Outline each blood parasite and name the species.
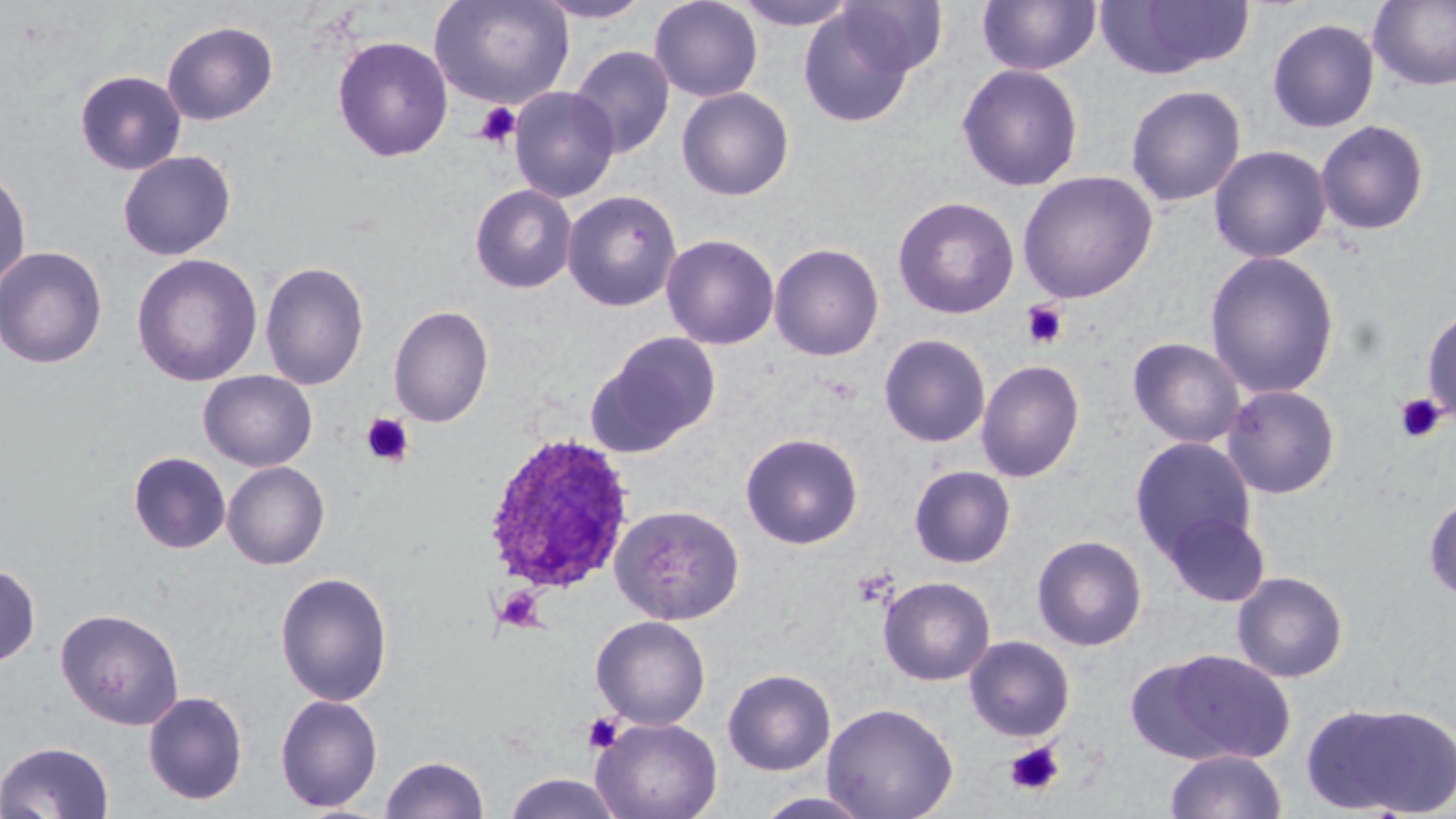
Approximate bounding boxes as named x1/y1/x2/y2 corners in pixels.
Plasmodium ovale-infected red blood cells: (x1=480, y1=432, x2=637, y2=599).
No Plasmodium falciparum, Plasmodium malariae, Plasmodium vivax, Babesia divergens, or Trypanosoma brucei observed.

slide_level_diagnosis: Plasmodium ovale
preparation: thin blood film
uninfected_red_blood_cell_locations: 'approximate bounding boxes as named x1/y1/x2/y2 corners in pixels: (x1=428, y1=0, x2=575, y2=109), (x1=532, y1=0, x2=653, y2=24), (x1=649, y1=0, x2=763, y2=102), (x1=734, y1=0, x2=860, y2=30), (x1=836, y1=0, x2=948, y2=79), (x1=977, y1=0, x2=1101, y2=76), (x1=1096, y1=0, x2=1254, y2=79), (x1=1368, y1=0, x2=1456, y2=91), (x1=797, y1=7, x2=916, y2=127), (x1=1267, y1=18, x2=1380, y2=133), (x1=162, y1=20, x2=278, y2=125), (x1=332, y1=35, x2=453, y2=162), (x1=569, y1=45, x2=675, y2=159), (x1=956, y1=63, x2=1084, y2=192), (x1=75, y1=70, x2=187, y2=175), (x1=1125, y1=84, x2=1246, y2=207), (x1=509, y1=86, x2=619, y2=203), (x1=676, y1=87, x2=795, y2=200), (x1=1315, y1=119, x2=1430, y2=236), (x1=1209, y1=145, x2=1331, y2=263), (x1=118, y1=150, x2=236, y2=261), (x1=0, y1=166, x2=31, y2=295), (x1=1017, y1=170, x2=1158, y2=304), (x1=470, y1=184, x2=577, y2=293), (x1=562, y1=190, x2=683, y2=312), (x1=892, y1=195, x2=1020, y2=319), (x1=661, y1=234, x2=780, y2=350), (x1=768, y1=242, x2=885, y2=361), (x1=0, y1=245, x2=108, y2=369), (x1=1204, y1=250, x2=1340, y2=399), (x1=131, y1=253, x2=263, y2=387), (x1=260, y1=260, x2=369, y2=390), (x1=1422, y1=303, x2=1456, y2=430), (x1=388, y1=305, x2=494, y2=427), (x1=588, y1=331, x2=723, y2=455), (x1=878, y1=333, x2=991, y2=448), (x1=1128, y1=337, x2=1245, y2=448), (x1=975, y1=359, x2=1086, y2=482), (x1=198, y1=370, x2=317, y2=471), (x1=1221, y1=384, x2=1341, y2=499), (x1=740, y1=432, x2=864, y2=550), (x1=1129, y1=437, x2=1257, y2=563), (x1=128, y1=451, x2=231, y2=554), (x1=222, y1=461, x2=330, y2=569), (x1=909, y1=465, x2=1016, y2=568), (x1=1423, y1=494, x2=1456, y2=602), (x1=609, y1=504, x2=745, y2=626), (x1=1161, y1=511, x2=1272, y2=606), (x1=1032, y1=534, x2=1147, y2=651), (x1=0, y1=561, x2=41, y2=668), (x1=1232, y1=570, x2=1349, y2=683), (x1=275, y1=571, x2=394, y2=707), (x1=878, y1=575, x2=995, y2=685), (x1=55, y1=607, x2=185, y2=730), (x1=591, y1=615, x2=711, y2=729), (x1=963, y1=635, x2=1075, y2=742), (x1=1151, y1=648, x2=1296, y2=763), (x1=723, y1=668, x2=836, y2=776), (x1=143, y1=690, x2=248, y2=805), (x1=275, y1=693, x2=383, y2=813), (x1=1304, y1=700, x2=1456, y2=817), (x1=822, y1=702, x2=959, y2=819), (x1=590, y1=717, x2=723, y2=819), (x1=0, y1=740, x2=114, y2=819), (x1=1164, y1=749, x2=1287, y2=819), (x1=380, y1=754, x2=489, y2=818), (x1=503, y1=773, x2=624, y2=819), (x1=752, y1=791, x2=876, y2=818)'
stain: May-Grünwald-Giemsa
image_size: 1456×819 pixels
magnification: 1000x
platelet_locations: 'approximate bounding boxes as named x1/y1/x2/y2 corners in pixels: (x1=474, y1=101, x2=522, y2=148), (x1=1021, y1=301, x2=1069, y2=350), (x1=1394, y1=392, x2=1448, y2=443), (x1=361, y1=413, x2=414, y2=467), (x1=494, y1=586, x2=546, y2=632), (x1=583, y1=712, x2=624, y2=753), (x1=1005, y1=742, x2=1064, y2=796)'
modality: light microscopy
field_of_view: single